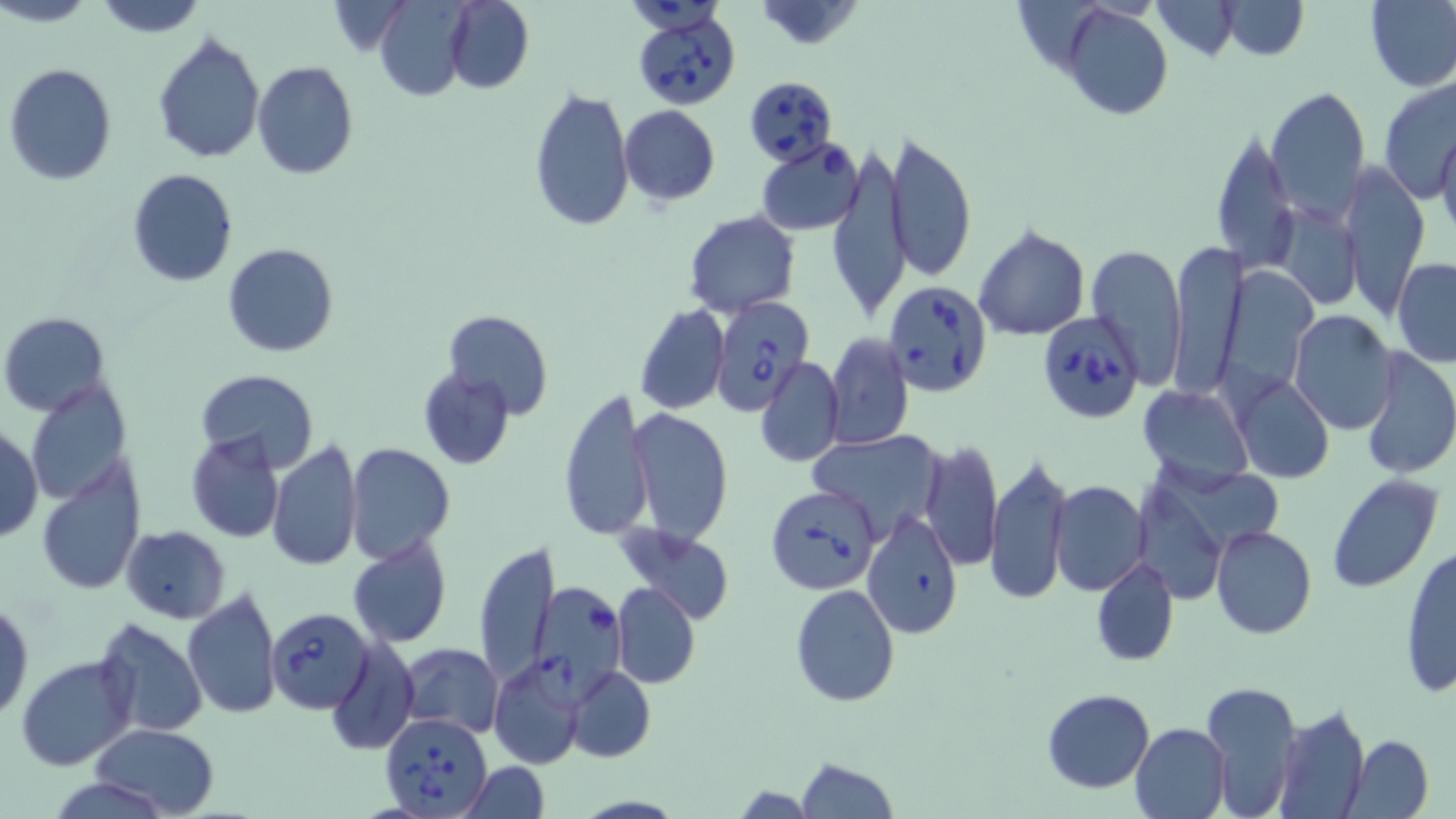
slide-level diagnosis = Babesia divergens
field of view = one of a larger specimen
magnification = 1000x
uninfected red blood cell locations = approximate bounding boxes as (x1,y1)-(x2,y2) corner pairs in pixels: (2,0)-(97,29), (90,0)-(209,37), (444,0)-(533,93), (754,0)-(870,52), (1152,0)-(1243,60), (1221,0)-(1307,59), (1365,0)-(1456,91), (373,4)-(472,102), (1063,4)-(1172,120), (152,32)-(266,161), (251,61)-(359,181), (4,63)-(117,185), (1377,74)-(1456,200), (1266,85)-(1370,223), (528,88)-(633,233), (619,105)-(719,204), (1211,126)-(1297,274), (1436,126)-(1456,242), (884,128)-(977,281), (828,146)-(911,323), (1338,166)-(1430,315), (125,167)-(240,288), (1276,203)-(1363,310), (683,210)-(801,316), (973,225)-(1090,340), (1170,239)-(1246,401), (222,243)-(338,358), (1085,245)-(1187,386), (1393,258)-(1456,367), (634,305)-(729,415), (442,308)-(552,419), (1288,309)-(1397,434), (1,312)-(113,417), (823,332)-(913,449), (1357,348)-(1456,481), (754,356)-(845,468), (416,367)-(516,469), (195,369)-(319,475), (1234,375)-(1333,484), (26,382)-(132,503), (1139,384)-(1253,490), (557,392)-(653,538), (629,409)-(733,544), (0,426)-(43,543), (807,430)-(948,538), (184,431)-(285,544), (919,439)-(1003,572), (266,441)-(364,570), (343,443)-(457,563), (985,455)-(1073,604), (36,460)-(146,595), (1327,473)-(1442,592), (1049,481)-(1149,596), (864,509)-(963,639), (120,525)-(231,622), (616,525)-(736,625), (1209,525)-(1316,640), (348,531)-(453,650), (472,540)-(558,688), (1399,545)-(1456,698), (1090,554)-(1179,667), (611,582)-(700,689), (790,583)-(899,705), (181,586)-(281,721), (1,596)-(34,723), (91,617)-(207,739), (325,634)-(419,754), (397,642)-(504,739), (16,655)-(137,771), (487,660)-(585,769), (567,666)-(656,763), (1202,680)-(1301,818), (1043,689)-(1155,793), (1273,703)-(1371,819), (1130,722)-(1231,819), (89,723)-(220,817), (1349,734)-(1434,818), (795,758)-(899,818), (460,760)-(551,818)
stain = May-Grünwald-Giemsa
image size = 1456×819 pixels
modality = light microscopy
Babesia divergens-infected red blood cell locations = approximate bounding boxes as (x1,y1)-(x2,y2) corner pairs in pixels: (629,7)-(740,112), (747,78)-(840,167), (757,140)-(865,236), (883,281)-(996,398), (709,296)-(818,418), (1037,311)-(1143,425), (766,485)-(881,596), (526,583)-(626,697), (269,607)-(374,713), (378,712)-(492,818)
preparation = thin blood film